Assess this cell for malaria.
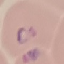
It is parasitized.

Summary:
  - Image type: cell patch, automatically extracted from a larger field of view and resized to 64 × 64 pixels
  - Stain: Giemsa
  - Capture: smartphone camera at the microscope eyepiece
  - Preparation: thin blood film